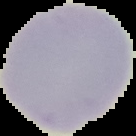 Image is 136×136 pixels. Malaria status: uninfected. From a thin blood smear. Cell region segmented out of the field of view; the surrounding area is masked to black.